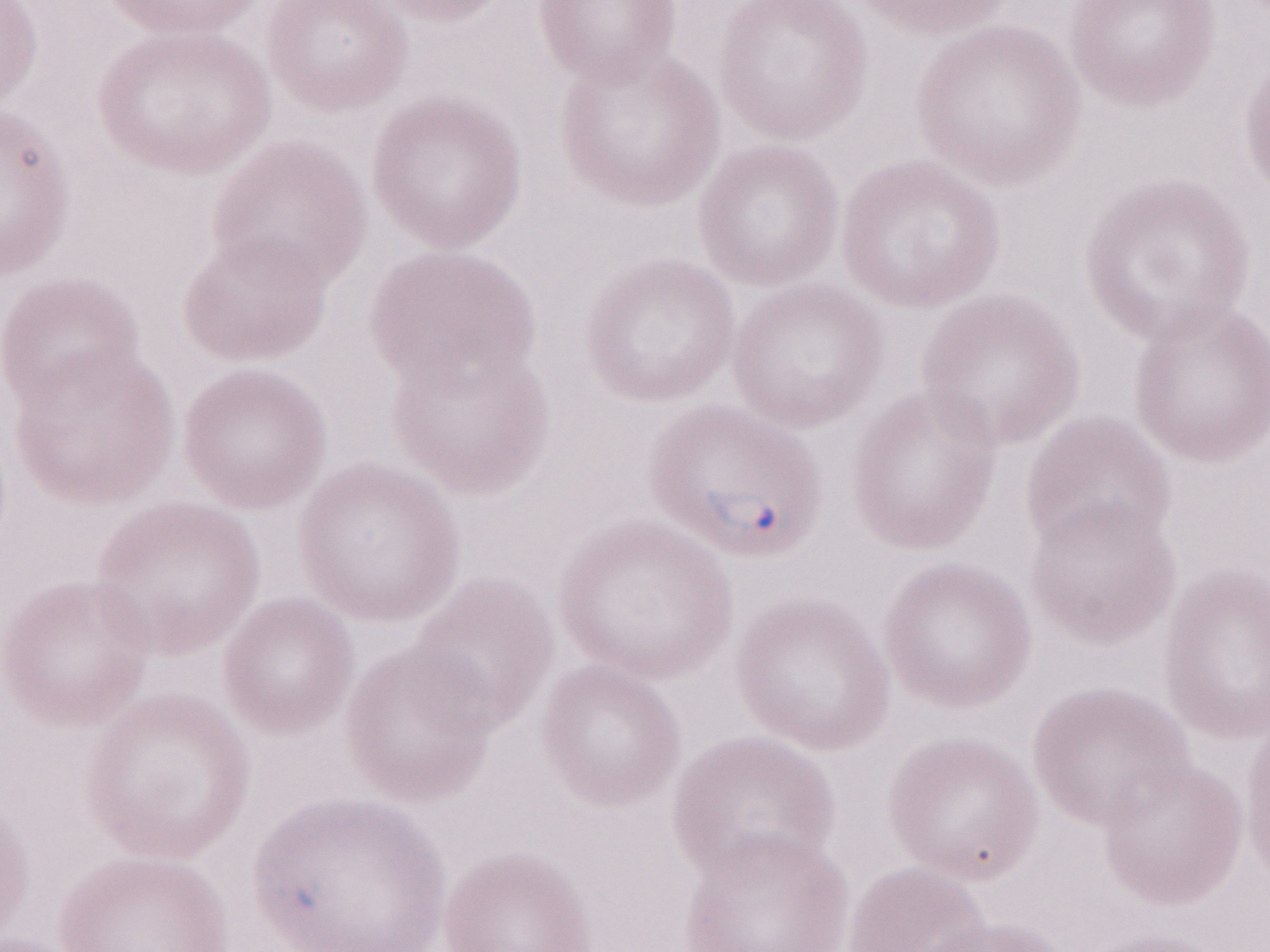 Thin blood film. Olympus BX43 microscope and DP73 digital camera. Patient diagnosis: malaria infection. Single field of view. Magnification: 1,000x. May-Grünwald-Giemsa-stained preparation. Image is 1270×952 pixels.